Describe the morphology of the red blood cells.
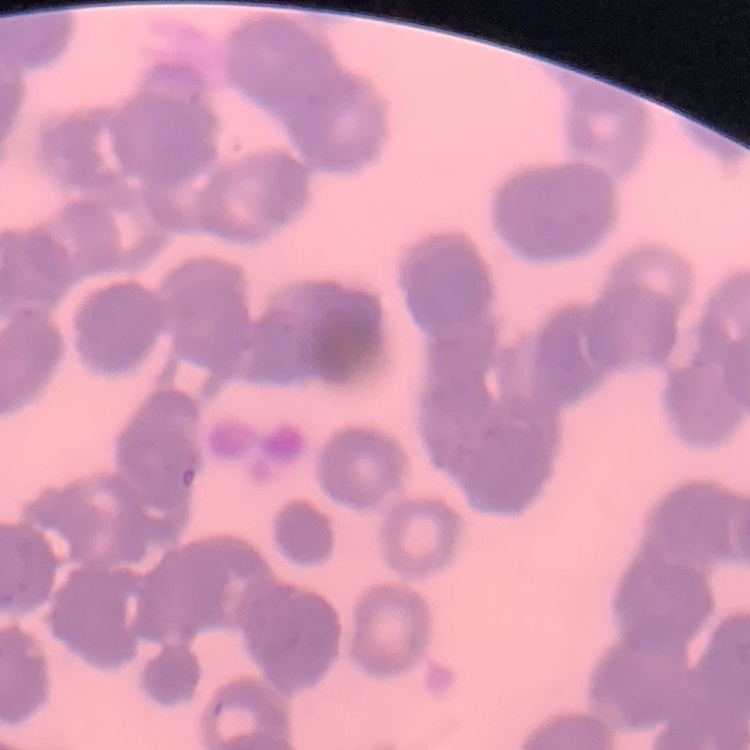
They show rouleaux formation.

One tile cut from a larger photomicrograph. Stained with either Field's or Giemsa. Thin blood film.